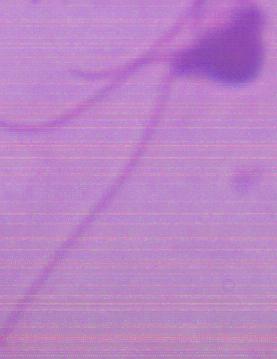
Photomicrograph. Captured at 1000x magnification. A Leishmania parasite is shown.